Classify this cell by malaria status.
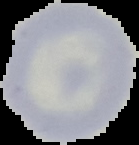

Uninfected.

Segmented cell region on a black background. Image is 139×145 pixels. From a thin blood film.